Identify the parasite.
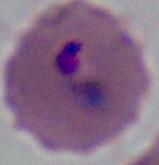

Plasmodium.

Summary:
  - Magnification: 400x or 1000x
  - Modality: micrograph